Name the cell type shown.
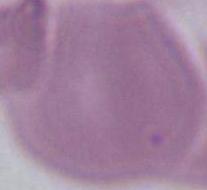
This is an erythrocyte.

magnification: 1000x
modality: micrograph